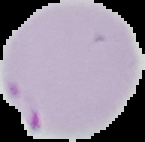

Result: malaria parasites identified. Image is 145×142 pixels. From a thin blood film. Cell region segmented out of the field of view; the surrounding area is masked to black.